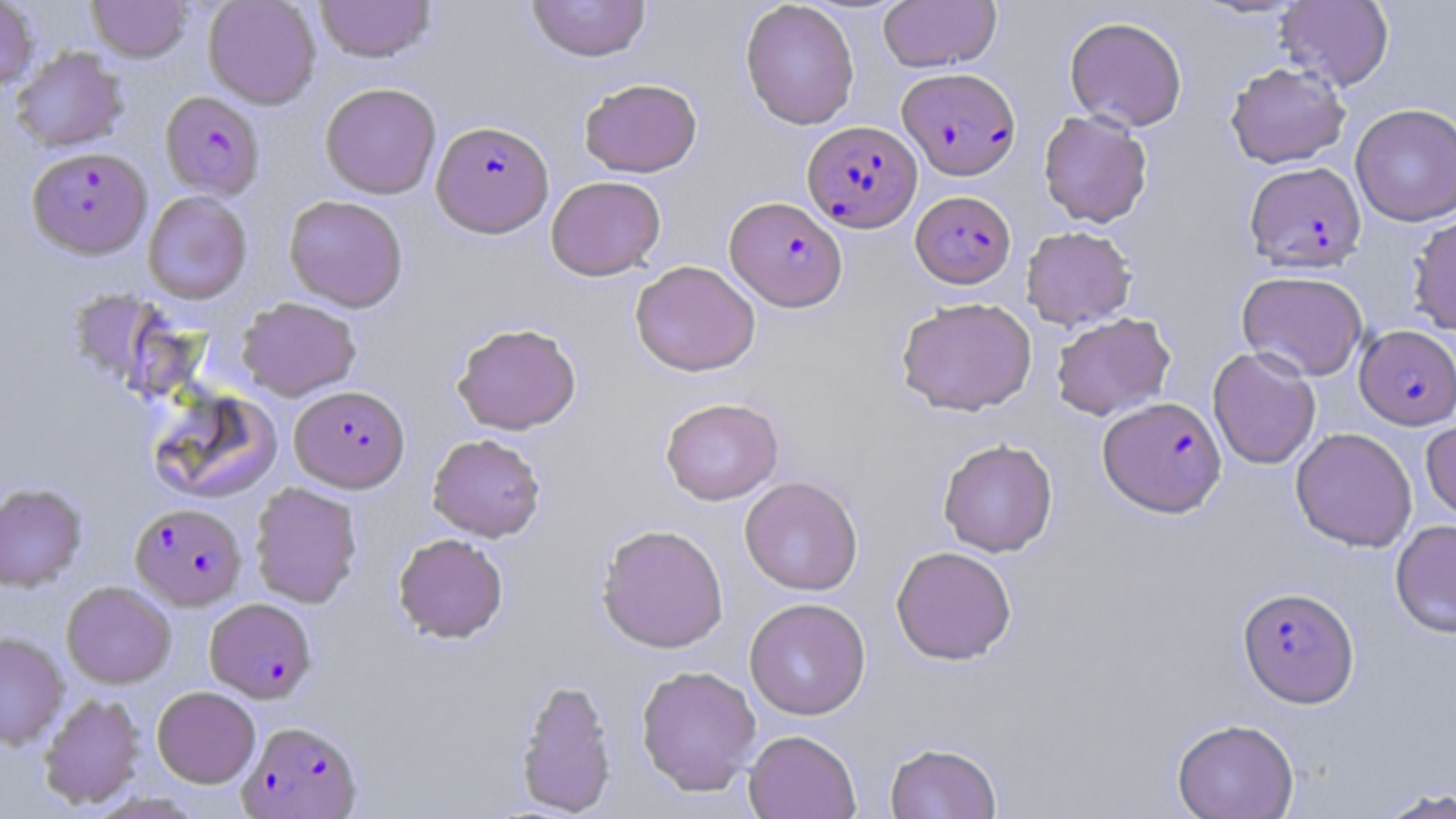
Summary:
  - Coordinate format: approximate bounding boxes as (x1, y1, x2, y2) in pixels
  - Uninfected red blood cell locations: (0, 0, 39, 90), (87, 0, 192, 62), (203, 0, 322, 109), (316, 0, 436, 62), (526, 0, 651, 62), (740, 0, 859, 130), (878, 0, 1001, 72), (1275, 1, 1394, 91), (1064, 16, 1188, 131), (10, 46, 129, 152), (1225, 62, 1350, 168), (579, 78, 703, 177), (320, 82, 441, 198), (1350, 103, 1456, 227), (1038, 110, 1153, 228), (546, 175, 666, 280), (143, 191, 252, 304), (284, 194, 409, 312), (1408, 213, 1456, 336), (1021, 225, 1136, 330), (630, 259, 760, 376), (1236, 270, 1368, 381), (237, 297, 361, 401), (896, 297, 1037, 416), (1051, 312, 1175, 420), (452, 322, 581, 434), (1207, 347, 1321, 470), (147, 387, 282, 504), (660, 397, 783, 505), (1421, 418, 1456, 526), (1290, 427, 1417, 552), (427, 433, 546, 542), (937, 438, 1058, 557), (739, 476, 863, 596), (0, 482, 87, 591), (249, 482, 362, 608), (1390, 519, 1456, 638), (596, 523, 729, 652), (393, 532, 508, 643), (891, 545, 1017, 665), (61, 581, 175, 688), (744, 597, 871, 720), (0, 631, 69, 750), (636, 664, 761, 796), (514, 677, 618, 816), (152, 686, 260, 787), (39, 692, 145, 809), (1171, 718, 1299, 819), (743, 729, 861, 818), (884, 741, 1002, 819), (1375, 786, 1456, 819)
  - Plasmodium falciparum-infected red blood cell locations: (897, 67, 1020, 180), (160, 91, 265, 199), (432, 120, 554, 236), (802, 120, 923, 232), (27, 146, 152, 258), (1244, 161, 1366, 273), (910, 190, 1016, 288), (725, 196, 848, 311), (1355, 325, 1456, 429), (290, 385, 410, 492), (1098, 396, 1227, 517), (131, 502, 246, 610), (1238, 586, 1359, 708), (204, 597, 317, 703), (238, 719, 364, 818)
  - Slide-level diagnosis: Plasmodium falciparum
  - Field of view: single
  - Stain: May-Grünwald-Giemsa
  - Image size: 1456×819 pixels
  - Modality: optical microscopy
  - Preparation: thin blood film
  - Magnification: 1000x